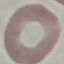

result: negative for malaria parasites
preparation: thin blood smear
capture: smartphone through the microscope eyepiece
stain: Giemsa
image_type: automatically extracted cell patch, resized to 64 × 64 pixels